Assess this cell for malaria.
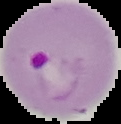
Parasitized.

{
  "image_type": "segmented cell region with the area outside set to black",
  "image_size": "121×124 pixels",
  "preparation": "thin blood smear"
}